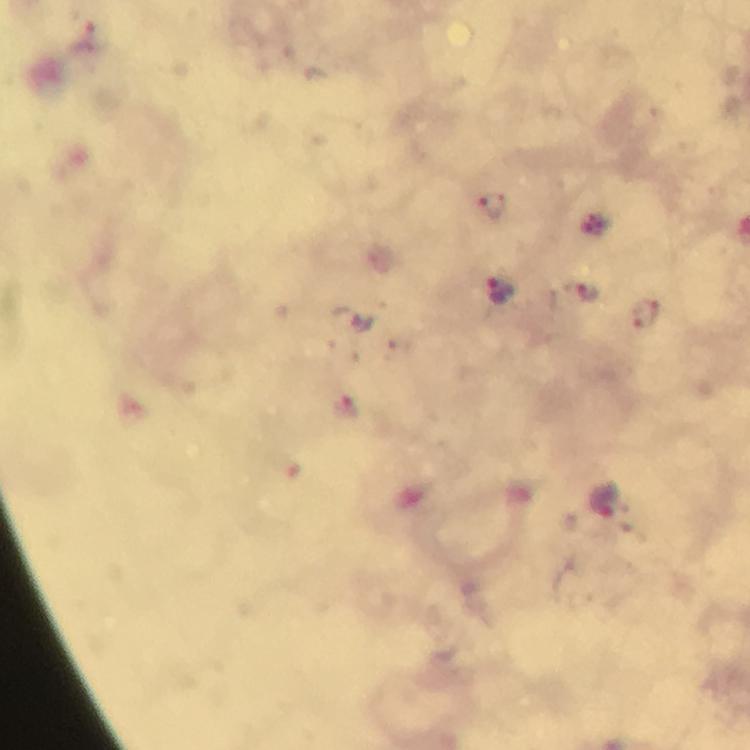
Approximate centers as {x, y} in pixels. Malaria parasite locations: {494, 208}, {584, 291}, {503, 292}, {646, 315}, {601, 500}. Immersion oil applied. Photographed with a smartphone mounted on the microscope. Cropped region of a single field of view. Thick smear. From a malaria diagnostic workup. 100x magnification. Giemsa stain. Image is 750×750 pixels.